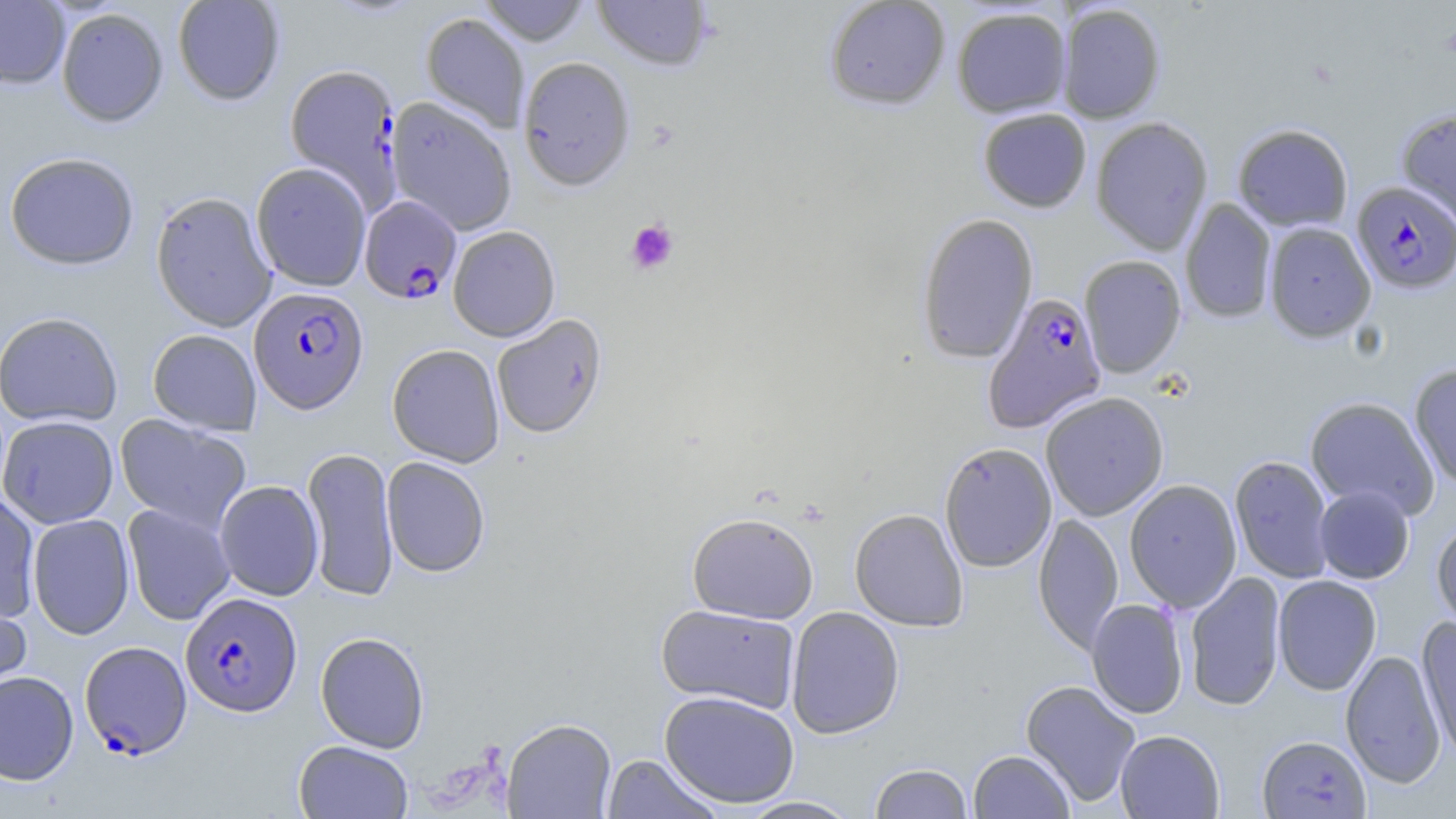
{
  "slide_level_diagnosis": "Plasmodium falciparum",
  "image_size": "1456×819 pixels",
  "modality": "optical microscopy",
  "field_of_view": "one of a larger specimen",
  "plasmodium_falciparum_infected_red_blood_cell_locations": "approximate bounding boxes as named x1/y1/x2/y2 corners in pixels: (x1=1352, y1=181, x2=1456, y2=293), (x1=359, y1=196, x2=461, y2=304), (x1=248, y1=286, x2=368, y2=414), (x1=982, y1=291, x2=1109, y2=431), (x1=180, y1=592, x2=302, y2=717), (x1=80, y1=641, x2=192, y2=759)",
  "uninfected_red_blood_cell_locations": "approximate bounding boxes as named x1/y1/x2/y2 corners in pixels: (x1=0, y1=0, x2=70, y2=89), (x1=172, y1=0, x2=286, y2=105), (x1=478, y1=0, x2=591, y2=46), (x1=592, y1=0, x2=714, y2=72), (x1=823, y1=0, x2=951, y2=110), (x1=1056, y1=4, x2=1165, y2=123), (x1=951, y1=6, x2=1072, y2=118), (x1=56, y1=7, x2=168, y2=127), (x1=421, y1=12, x2=530, y2=134), (x1=517, y1=56, x2=636, y2=191), (x1=284, y1=63, x2=402, y2=204), (x1=386, y1=97, x2=517, y2=236), (x1=1397, y1=107, x2=1456, y2=229), (x1=977, y1=108, x2=1092, y2=212), (x1=1090, y1=116, x2=1214, y2=255), (x1=1233, y1=124, x2=1353, y2=231), (x1=4, y1=152, x2=140, y2=270), (x1=251, y1=162, x2=372, y2=291), (x1=150, y1=191, x2=277, y2=332), (x1=1180, y1=198, x2=1277, y2=323), (x1=916, y1=212, x2=1038, y2=363), (x1=1263, y1=222, x2=1376, y2=342), (x1=447, y1=225, x2=561, y2=342), (x1=1079, y1=255, x2=1186, y2=377), (x1=0, y1=311, x2=123, y2=428), (x1=491, y1=314, x2=607, y2=438), (x1=147, y1=329, x2=262, y2=434), (x1=387, y1=343, x2=505, y2=467), (x1=1408, y1=363, x2=1456, y2=488), (x1=1040, y1=391, x2=1169, y2=520), (x1=1305, y1=397, x2=1440, y2=519), (x1=115, y1=414, x2=252, y2=534), (x1=0, y1=415, x2=119, y2=528), (x1=939, y1=441, x2=1057, y2=572), (x1=302, y1=447, x2=399, y2=602), (x1=1229, y1=455, x2=1335, y2=584), (x1=381, y1=456, x2=490, y2=577), (x1=1124, y1=479, x2=1242, y2=612), (x1=214, y1=480, x2=324, y2=601), (x1=1314, y1=485, x2=1414, y2=584), (x1=0, y1=491, x2=42, y2=622), (x1=122, y1=504, x2=235, y2=625), (x1=849, y1=508, x2=969, y2=632), (x1=687, y1=512, x2=819, y2=624), (x1=1033, y1=512, x2=1123, y2=655), (x1=27, y1=513, x2=135, y2=639), (x1=1432, y1=520, x2=1456, y2=634), (x1=1183, y1=571, x2=1286, y2=711), (x1=1272, y1=575, x2=1381, y2=696), (x1=0, y1=589, x2=32, y2=706), (x1=1086, y1=598, x2=1189, y2=719), (x1=655, y1=603, x2=801, y2=714), (x1=785, y1=606, x2=905, y2=739), (x1=1417, y1=616, x2=1456, y2=761), (x1=315, y1=631, x2=430, y2=753), (x1=1340, y1=650, x2=1446, y2=788), (x1=0, y1=670, x2=79, y2=786), (x1=1020, y1=679, x2=1141, y2=807), (x1=659, y1=690, x2=800, y2=808), (x1=502, y1=718, x2=616, y2=818), (x1=1115, y1=729, x2=1225, y2=818), (x1=1257, y1=734, x2=1371, y2=818), (x1=293, y1=740, x2=413, y2=819), (x1=968, y1=749, x2=1074, y2=819), (x1=601, y1=753, x2=724, y2=818), (x1=870, y1=762, x2=973, y2=818), (x1=735, y1=796, x2=863, y2=818)",
  "platelet_locations": "approximate bounding boxes as named x1/y1/x2/y2 corners in pixels: (x1=625, y1=218, x2=679, y2=275)",
  "stain": "May-Grünwald-Giemsa",
  "preparation": "thin blood smear",
  "magnification": "1000x"
}